Identify the parasite.
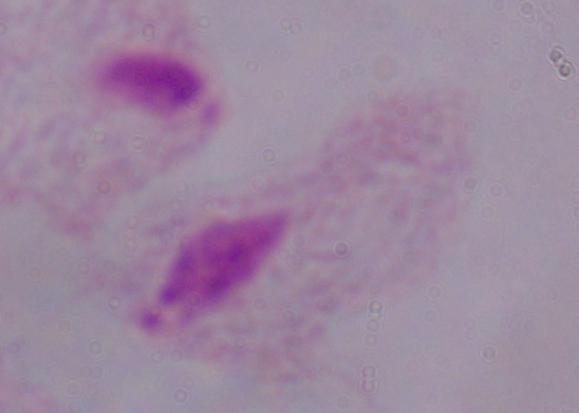

This is a trichomonad.

Summary:
  - Modality: photomicrograph
  - Magnification: 1000x